Give the position of every Plasmodium parasite.
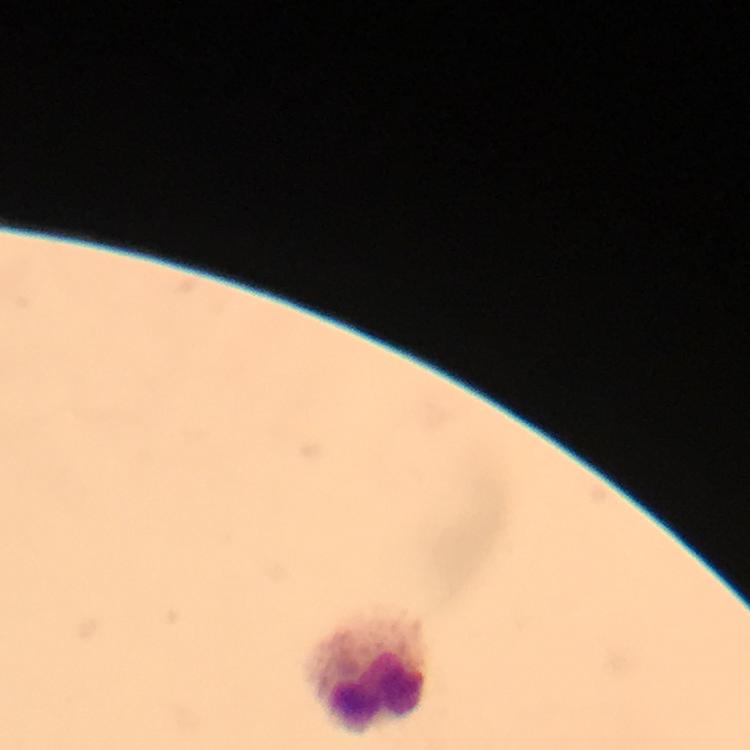

No Plasmodium parasites seen.

context = from a malaria diagnostic workup
preparation = thick blood smear
capture = smartphone camera through the microscope
leukocyte locations = approximate centers as (x, y) in pixels: (365, 670)
cropped from = one field of view
immersion oil = used
stain = Giemsa
magnification = 100x
image size = 750×750 pixels